Assess this cell for malaria.
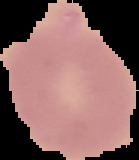

Uninfected.

{
  "image_size": "139×160 pixels",
  "image_type": "segmented cell region with the area outside set to black",
  "preparation": "thin blood smear"
}